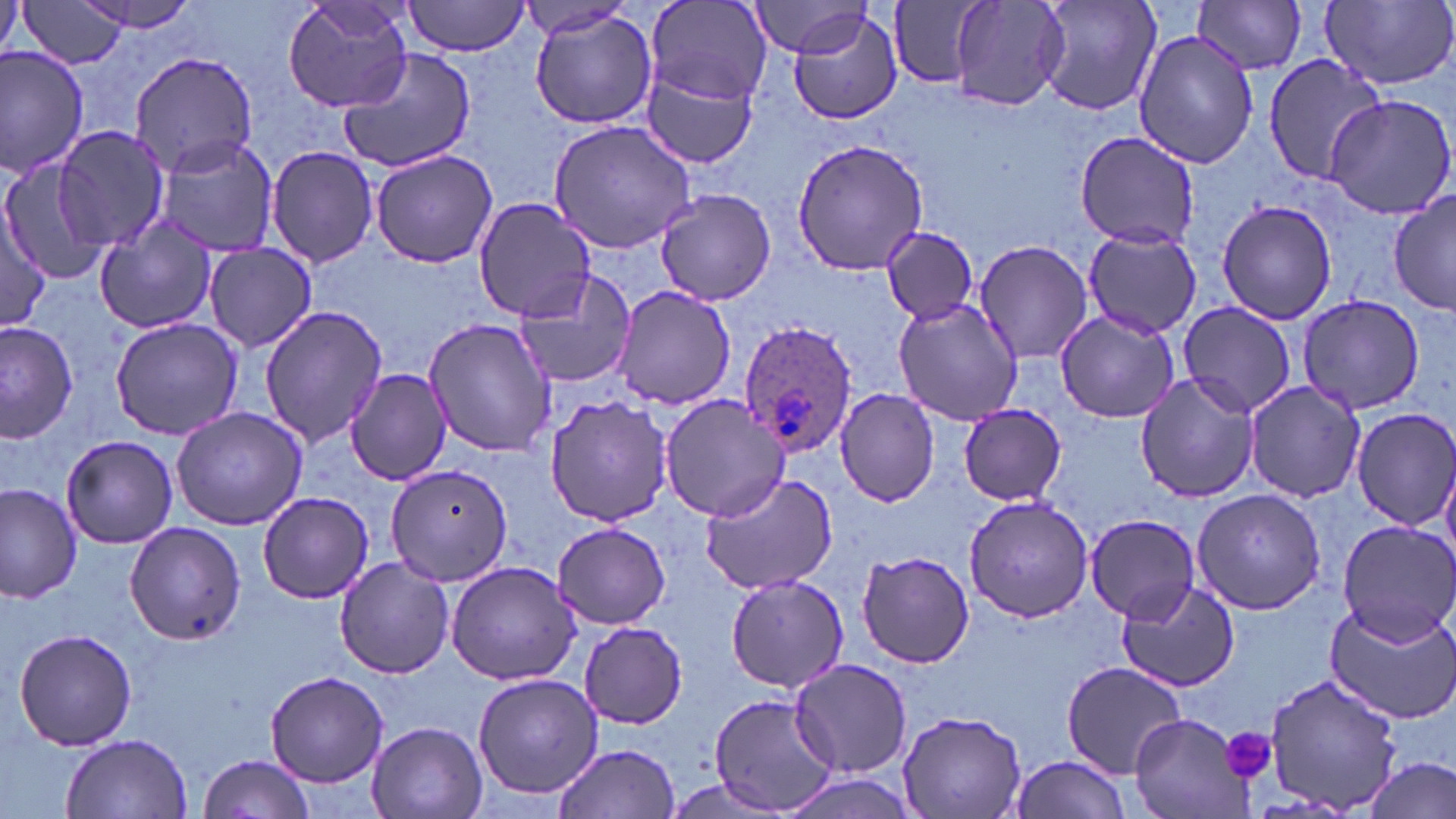
slide-level diagnosis = Plasmodium ovale
image size = 1456×819 pixels
platelet locations = approximate bounding boxes as (x1,y1)-(x2,y2) corner pairs in pixels: (1221,727)-(1278,783)
Plasmodium ovale-infected red blood cell locations = approximate bounding boxes as (x1,y1)-(x2,y2) corner pairs in pixels: (736,321)-(860,459)
uninfected red blood cell locations = approximate bounding boxes as (x1,y1)-(x2,y2) corner pairs in pixels: (16,0)-(129,69), (68,0)-(206,37), (279,0)-(417,114), (402,0)-(530,57), (950,0)-(1070,111), (1032,0)-(1164,118), (1192,0)-(1310,75), (1320,0)-(1456,90), (647,2)-(772,107), (889,2)-(984,88), (744,3)-(877,59), (518,5)-(634,39), (526,6)-(660,132), (787,7)-(903,127), (1133,28)-(1258,170), (0,44)-(91,178), (129,50)-(260,176), (338,50)-(479,173), (1262,52)-(1390,185), (643,64)-(760,170), (1324,94)-(1456,219), (548,116)-(700,254), (55,127)-(172,250), (1073,131)-(1201,249), (154,136)-(281,256), (792,138)-(928,275), (266,144)-(379,269), (368,148)-(498,268), (0,160)-(112,286), (653,187)-(776,306), (1389,191)-(1455,317), (471,197)-(597,323), (1215,199)-(1338,323), (0,208)-(52,333), (93,219)-(219,336), (882,227)-(978,322), (1081,227)-(1201,338), (973,239)-(1094,363), (203,243)-(317,351), (512,272)-(637,390), (611,284)-(739,409), (1295,293)-(1428,416), (891,297)-(1024,426), (1178,300)-(1296,419), (258,306)-(388,449), (1053,308)-(1179,422), (109,317)-(243,442), (424,317)-(555,458), (0,323)-(78,443), (346,367)-(452,485), (1134,373)-(1258,501), (1242,380)-(1365,501), (834,388)-(940,507), (544,394)-(672,527), (657,394)-(790,523), (958,404)-(1070,507), (171,406)-(308,531), (1350,407)-(1456,531), (61,434)-(179,549), (385,464)-(515,585), (699,468)-(839,594), (0,482)-(82,604), (1191,487)-(1328,614), (257,490)-(373,603), (962,495)-(1096,624), (1084,513)-(1203,623), (1337,519)-(1456,645), (123,521)-(248,645), (552,521)-(671,631), (855,550)-(976,668), (334,555)-(453,677), (445,560)-(583,684), (723,573)-(852,694), (1115,580)-(1242,692), (1324,603)-(1456,723), (578,621)-(688,728), (13,628)-(140,751), (789,659)-(912,778), (1060,661)-(1188,777), (264,671)-(390,787), (472,672)-(604,799), (1261,672)-(1405,816), (709,693)-(840,816), (897,709)-(1028,819), (1128,713)-(1250,819), (367,721)-(488,819), (62,733)-(191,818), (552,741)-(680,819), (198,753)-(315,819), (1005,754)-(1134,819), (1361,756)-(1456,819), (778,772)-(924,819)
stain = May-Grünwald-Giemsa
modality = light microscopy
field of view = single
preparation = thin blood film
magnification = 1000x